State the preparation type.
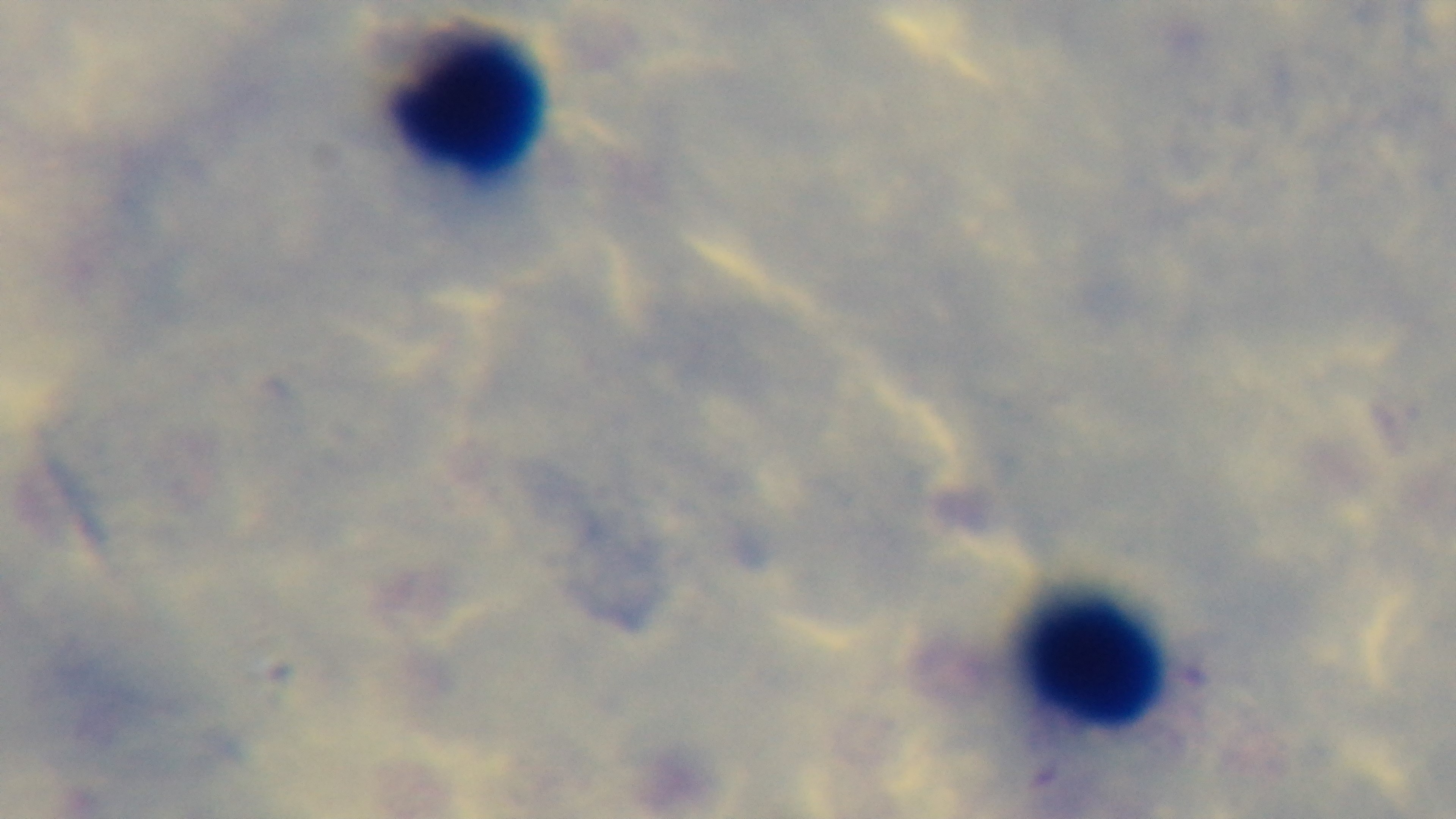

A thick smear.

{
  "malaria_status": "uninfected",
  "field_of_view": "one from the slide",
  "modality": "light microscopy",
  "capture": "mounted 4K digital camera",
  "stain": "Giemsa",
  "objective": "100x oil immersion"
}